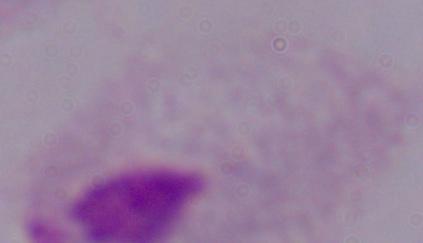
A trichomonad is shown. Micrograph. 1000x magnification.